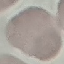
Summary:
  - Malaria status: uninfected
  - Capture: smartphone camera at the microscope eyepiece
  - Stain: Giemsa
  - Preparation: thin blood smear
  - Image type: automatically extracted cell patch, resized to 64 × 64 pixels